Report the malaria status of this cell.
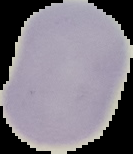

It is uninfected.

preparation = thin blood smear
image size = 133×154 pixels
image type = cell region segmented out of the field of view; surrounding area masked to black